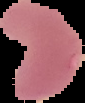

image type = cell region segmented out of the field of view; surrounding area masked to black
preparation = thin blood smear
result = malaria parasites detected
image size = 85×103 pixels